Assess the morphology of the red blood cells.
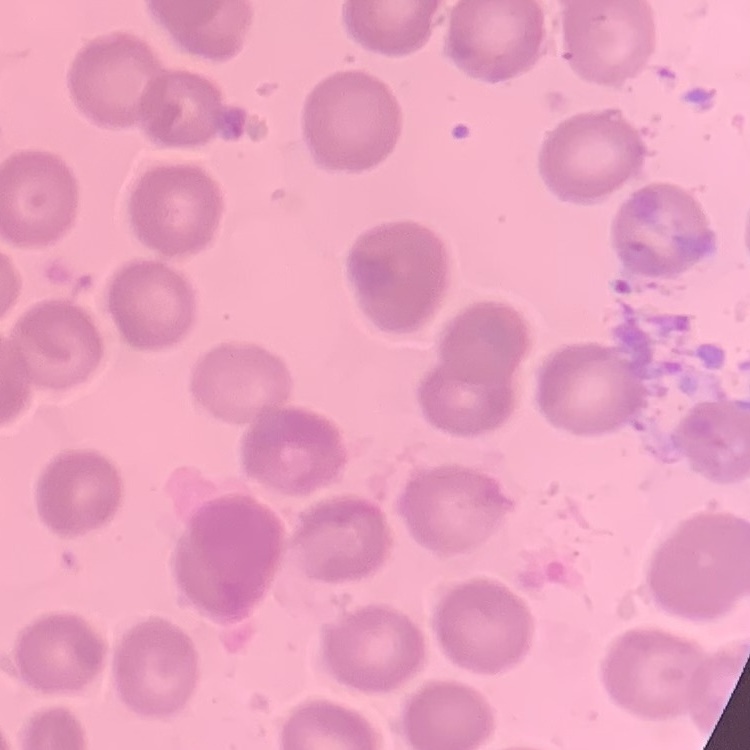

No rouleaux formation.

One tile cut from a larger photomicrograph. Thin blood film. Stained with either Field's or Giemsa.